Locate and identify every blood parasite.
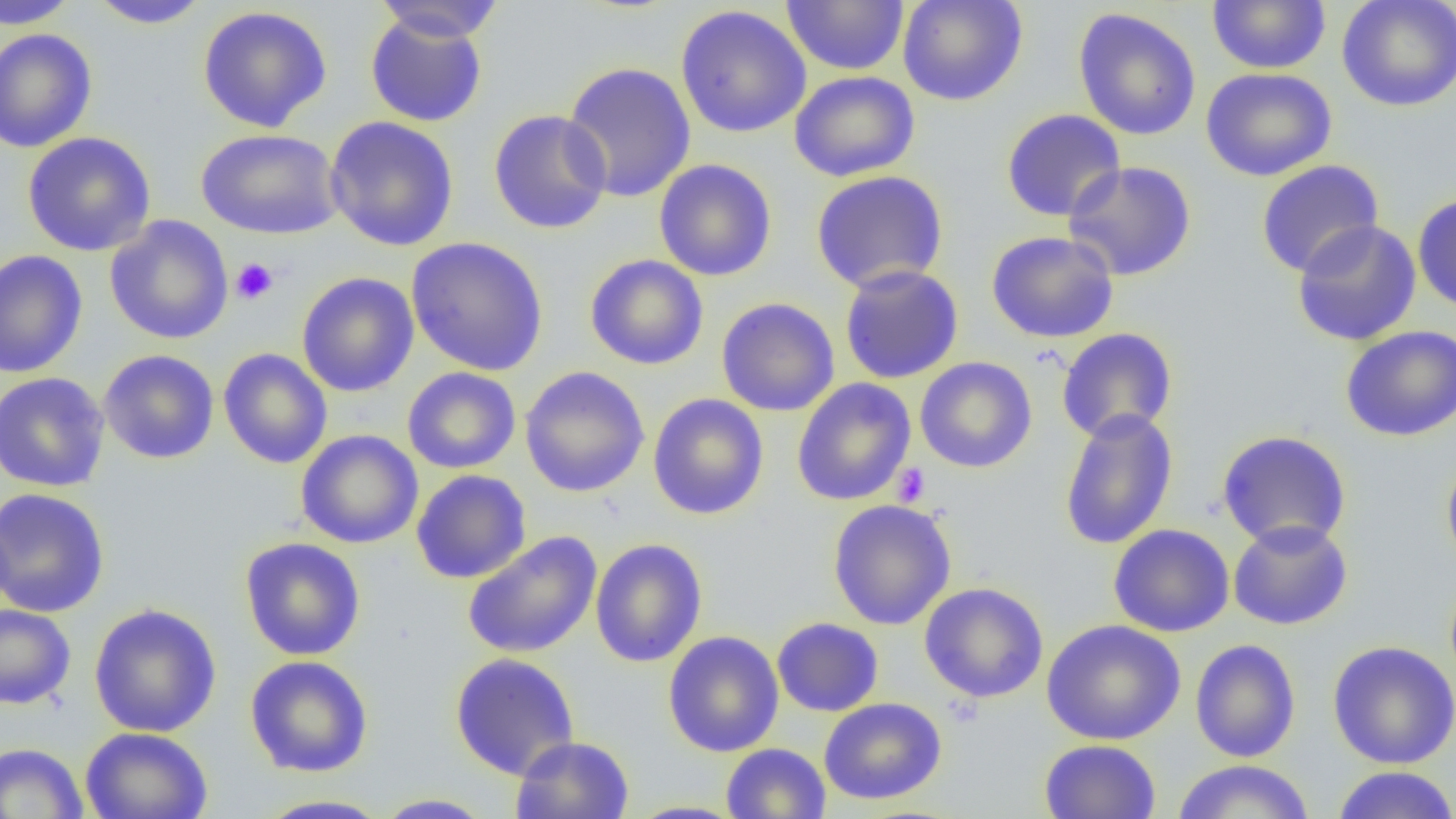

No blood parasites seen.

Approximate bounding boxes as (x1, y1, x2, y2) in pixels. Uninfected red blood cell locations: (0, 0, 80, 29), (87, 0, 212, 29), (781, 0, 909, 75), (897, 0, 1028, 106), (1337, 0, 1456, 112), (370, 1, 506, 42), (1207, 1, 1331, 73), (196, 5, 333, 132), (675, 5, 812, 139), (1073, 7, 1201, 141), (365, 11, 488, 127), (0, 28, 98, 153), (562, 61, 697, 203), (1201, 67, 1337, 182), (789, 71, 920, 182), (488, 109, 613, 234), (1001, 109, 1126, 222), (324, 116, 459, 251), (196, 128, 342, 240), (22, 131, 156, 256), (654, 159, 777, 281), (1256, 159, 1384, 278), (1063, 161, 1197, 281), (810, 170, 949, 293), (1413, 193, 1456, 314), (104, 216, 234, 345), (1291, 218, 1422, 347), (986, 230, 1119, 343), (406, 236, 549, 376), (0, 249, 88, 379), (584, 254, 709, 370), (839, 265, 964, 384), (297, 272, 419, 397), (716, 297, 840, 416), (1340, 325, 1456, 442), (1057, 328, 1178, 442), (218, 348, 333, 469), (99, 349, 220, 464), (915, 356, 1037, 473), (520, 366, 650, 497), (402, 367, 521, 473), (0, 372, 110, 492), (792, 377, 916, 506), (648, 393, 769, 520), (1059, 407, 1178, 551), (296, 430, 424, 549), (1216, 430, 1352, 550), (1441, 452, 1456, 574), (412, 469, 531, 584), (0, 487, 110, 618), (827, 499, 957, 630), (1228, 519, 1353, 631), (1108, 523, 1235, 637), (462, 531, 602, 659), (239, 537, 366, 661), (590, 538, 707, 667), (919, 582, 1049, 703), (88, 603, 222, 737), (0, 604, 76, 710), (772, 617, 884, 717), (1041, 618, 1185, 745), (663, 630, 784, 757), (1190, 639, 1301, 762), (1327, 640, 1456, 769), (449, 652, 580, 780), (245, 655, 373, 777), (819, 697, 947, 805), (80, 727, 213, 819), (510, 735, 635, 819), (1039, 739, 1161, 819), (0, 742, 89, 819), (720, 743, 831, 819), (1171, 759, 1316, 818), (1330, 766, 1456, 819), (373, 793, 496, 818), (251, 794, 396, 818), (624, 800, 748, 818). Platelet locations: (230, 257, 279, 304), (892, 463, 930, 506). Slide-level diagnosis: negative for blood parasites. Optical microscopy. Image is 1456×819 pixels. Single field of view. Thin blood smear. Captured at 1000x magnification.